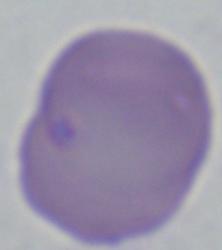

identification: Babesia
modality: micrograph
magnification: 1000x